Locate every Plasmodium ovale-infected red blood cell.
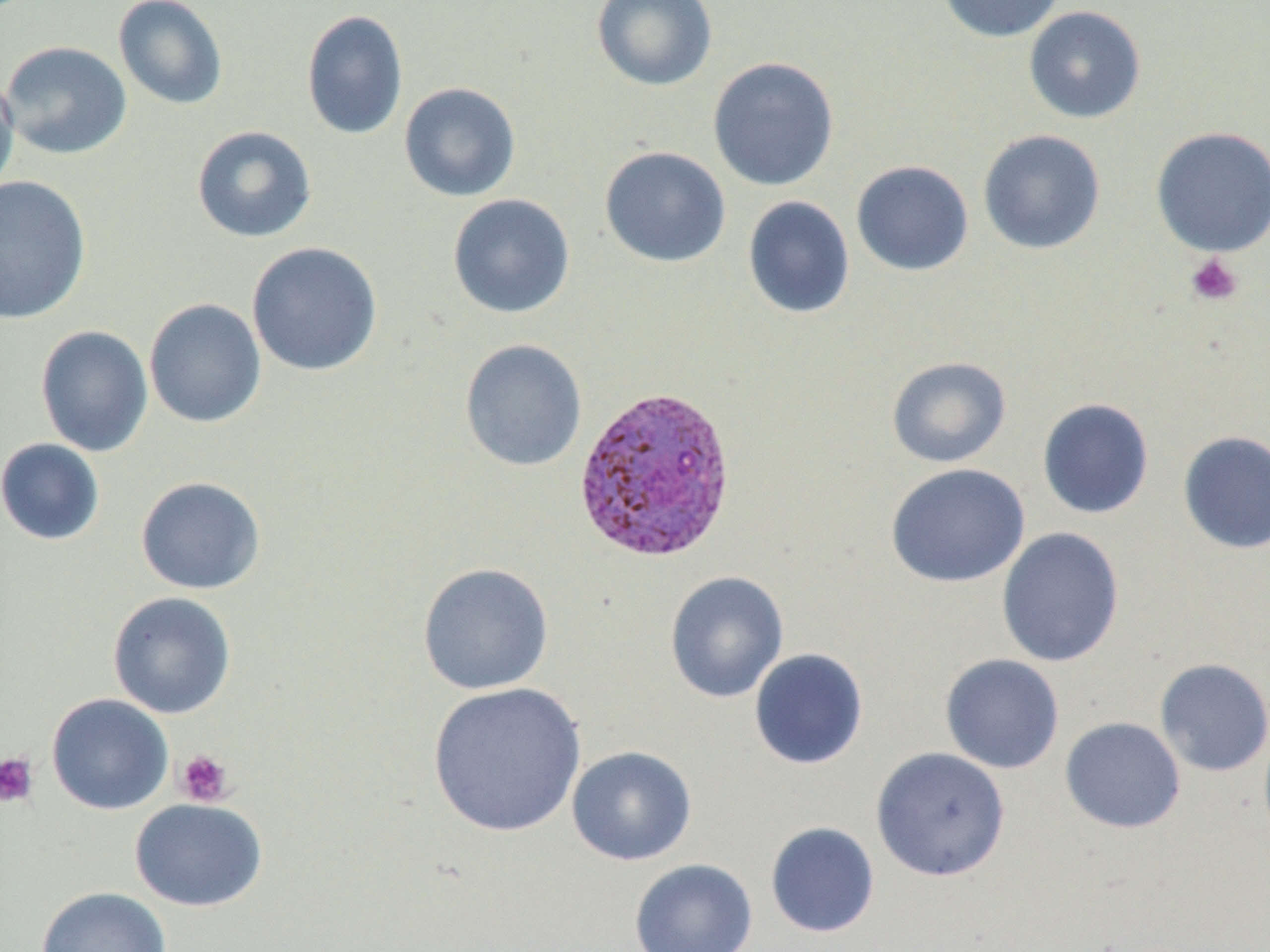

Approximate bounding boxes as (x1,y1)-(x2,y2) corner pairs in pixels.
Plasmodium ovale-infected red blood cells: (572,384)-(738,563).

slide-level diagnosis = Plasmodium ovale
image size = 1270×952 pixels
stain = May-Grünwald-Giemsa
modality = optical microscopy
preparation = thin blood smear
field of view = one of a larger specimen
uninfected red blood cell locations = approximate bounding boxes as (x1,y1)-(x2,y2) corner pairs in pixels: (112,0)-(228,110), (591,0)-(717,91), (935,0)-(1066,43), (1023,6)-(1146,124), (301,10)-(408,140), (1,40)-(133,160), (707,56)-(840,192), (0,69)-(20,199), (398,81)-(521,202), (191,126)-(317,243), (1150,126)-(1270,257), (978,129)-(1106,255), (599,146)-(731,268), (851,160)-(973,276), (0,176)-(91,325), (447,193)-(575,319), (742,195)-(855,319), (246,241)-(383,376), (144,298)-(266,428), (35,325)-(153,457), (459,339)-(587,472), (886,356)-(1012,468), (1037,398)-(1155,519), (1177,430)-(1270,554), (0,438)-(105,546), (885,463)-(1030,589), (135,476)-(266,595), (996,526)-(1125,668), (417,562)-(554,696), (665,571)-(788,703), (107,591)-(237,719), (748,648)-(869,770), (940,653)-(1064,774), (1154,658)-(1270,777), (427,682)-(587,837), (46,693)-(174,815), (1060,717)-(1186,834), (566,746)-(697,865), (871,747)-(1011,882), (130,798)-(267,912), (765,821)-(880,938), (629,859)-(757,952), (36,886)-(172,952)
magnification = 1000x
platelet locations = approximate bounding boxes as (x1,y1)-(x2,y2) corner pairs in pixels: (1185,253)-(1244,307), (175,749)-(234,807), (0,752)-(39,808)